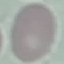
result = no malaria parasites seen
capture = smartphone through the microscope eyepiece
image type = cell patch, automatically extracted from a larger field of view and resized to 64 × 64 pixels
stain = Giemsa
preparation = thin blood film